Point out each Plasmodium parasite.
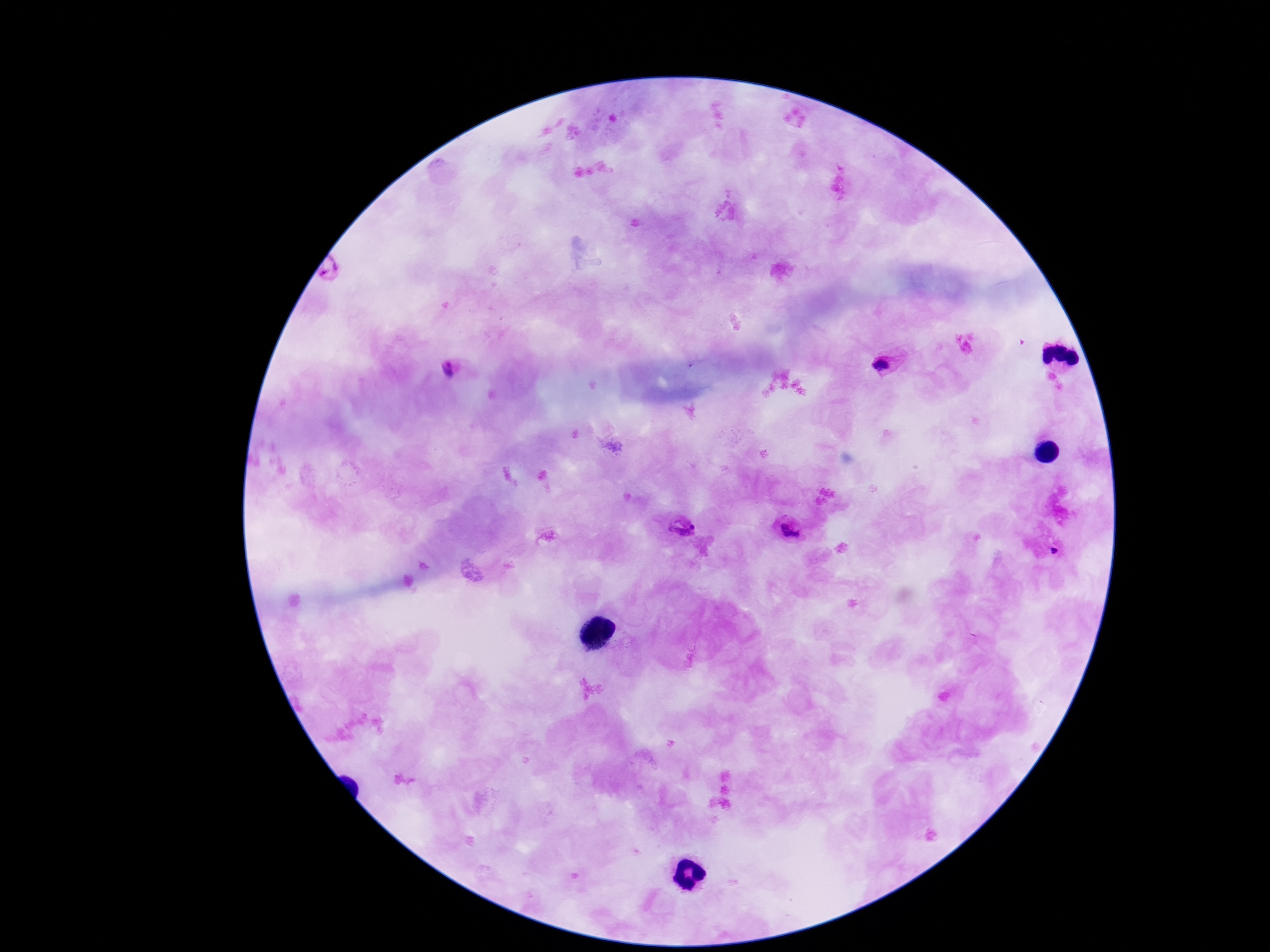
Approximate centers as [x, y] in pixels.
Plasmodium parasites: [330, 273], [884, 364], [451, 371], [682, 526], [790, 531].

field of view = one from this slide
image size = 1270×952 pixels
capture = smartphone camera through the microscope eyepiece
stain = Giemsa
magnification = 100x
patient malaria status = infected
preparation = thick blood smear